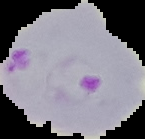
From a thin blood film. Image is 145×139 pixels. Malaria status: parasitized. Segmented cell region on a black background.